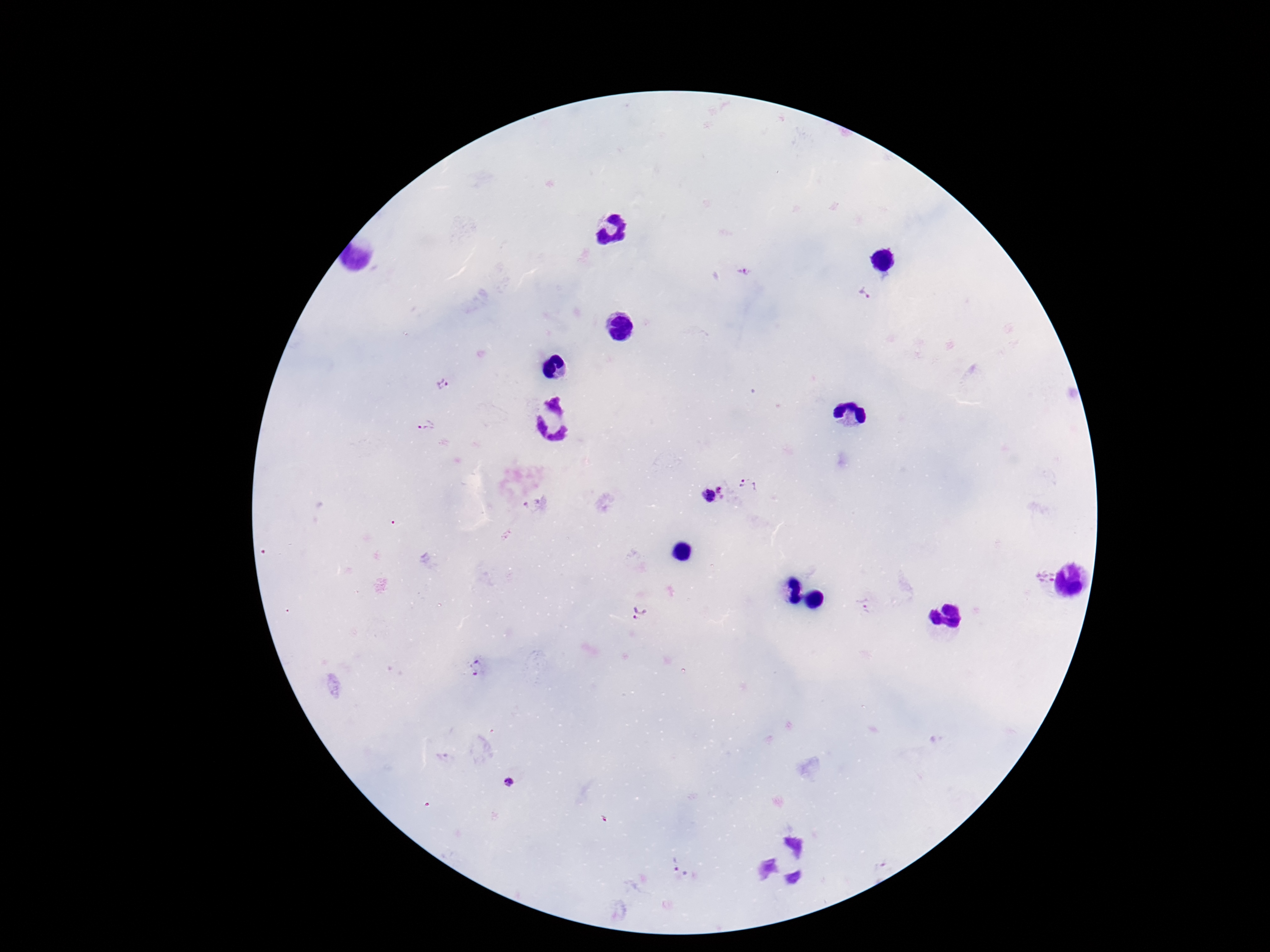

Approximate centers as {x, y} in pixels.
Summary:
  - Plasmodium parasite locations: {744, 271}, {864, 292}, {442, 385}, {426, 427}, {750, 484}, {724, 487}, {707, 496}, {530, 501}, {1043, 575}, {862, 608}, {638, 612}, {477, 669}, {509, 781}, {675, 863}, {690, 876}
  - Image size: 1270×952 pixels
  - Preparation: thick blood film
  - Patient malaria status: positive
  - Stain: Giemsa
  - Field of view: single
  - Capture: smartphone camera through the microscope eyepiece
  - Magnification: 100x